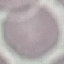

malaria status = uninfected
preparation = thin blood film
capture = smartphone camera at the microscope eyepiece
image type = cell patch, automatically extracted from a larger field of view and resized to 64 × 64 pixels
stain = Giemsa